State the preparation type.
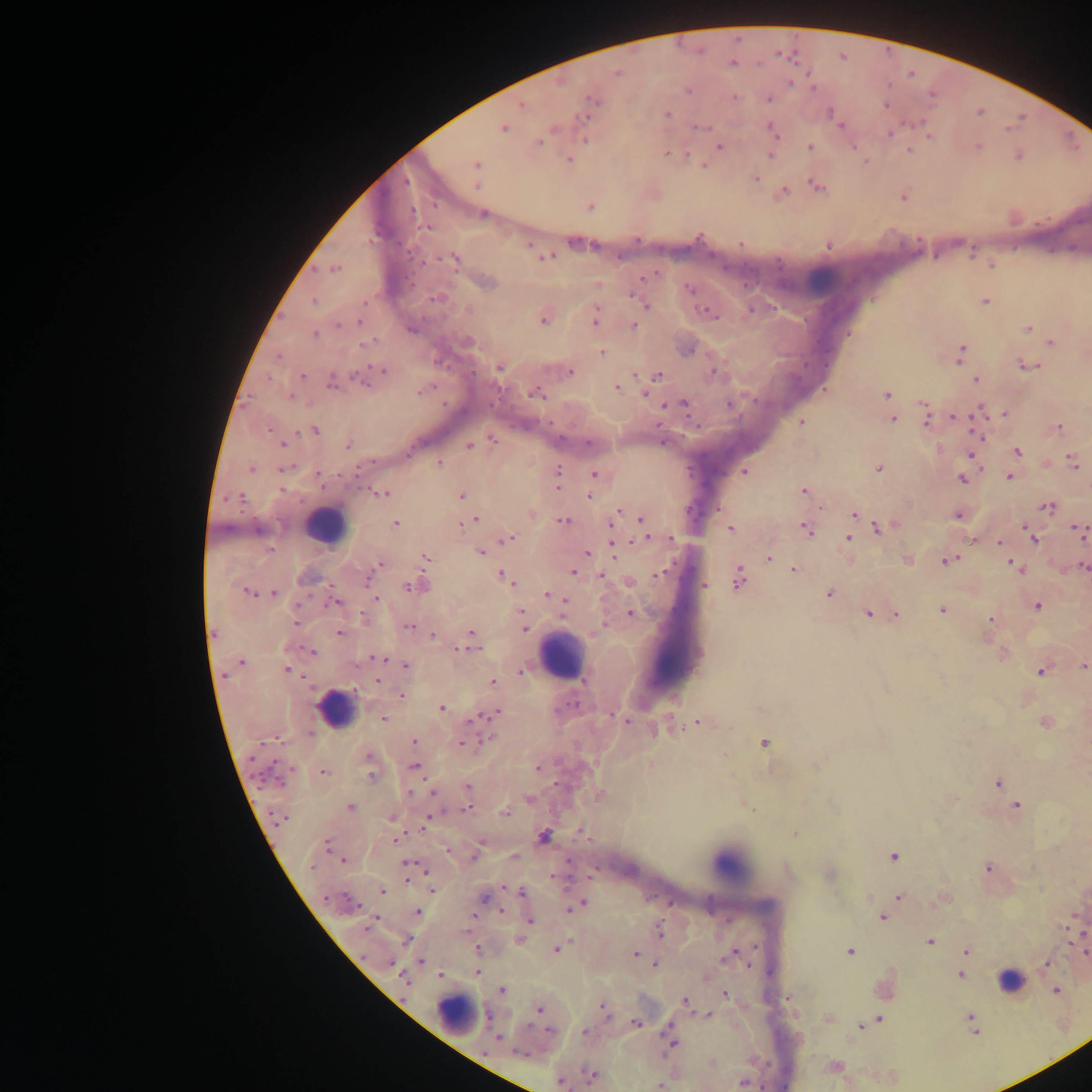

Thick blood film.

Approximate centers as [x, y] in pixels.
Summary:
  - Leukocyte locations: [823, 276], [327, 527], [561, 656], [663, 661], [335, 709], [732, 863], [1008, 979], [457, 1015]
  - Plasmodium parasite locations: [733, 63], [617, 74], [911, 74], [789, 83], [688, 90], [734, 97], [769, 99], [592, 101], [886, 104], [522, 105], [589, 109], [979, 112], [831, 113], [668, 115], [840, 125], [700, 127], [553, 128], [504, 129], [773, 131], [891, 132], [930, 137], [584, 139], [539, 141], [719, 146], [978, 146], [809, 147], [909, 150], [667, 153], [770, 155], [1019, 156], [569, 159], [476, 164], [702, 165], [756, 178], [477, 184], [817, 186], [784, 191], [903, 197], [590, 205], [412, 211], [483, 214], [427, 228], [579, 243], [529, 244], [828, 246], [544, 257], [454, 258], [335, 269], [648, 275], [487, 283], [690, 289], [436, 298], [314, 301], [985, 301], [645, 305], [707, 312], [595, 318], [543, 320], [359, 321], [339, 326], [633, 326], [1028, 328], [412, 329], [314, 334], [468, 341], [366, 343], [1051, 343], [961, 352], [601, 353], [1027, 366], [499, 368], [383, 371], [570, 372], [714, 372], [658, 375], [302, 376], [976, 380], [332, 382], [362, 382], [617, 387], [423, 391], [537, 393], [644, 394], [887, 394], [291, 397], [683, 404], [729, 404], [668, 405], [923, 406], [979, 411], [1005, 414], [892, 418], [955, 418], [926, 421], [800, 422], [1059, 428], [315, 430], [978, 435], [492, 440], [589, 443], [282, 444], [348, 445], [469, 445], [1017, 451], [972, 456], [1072, 462], [440, 464], [251, 469], [282, 469], [878, 469], [744, 472], [558, 474], [595, 474], [1009, 477], [962, 480], [804, 491], [382, 493], [461, 495], [239, 497], [589, 497], [1048, 507], [618, 513], [855, 513], [959, 515], [474, 520], [563, 521], [643, 521], [395, 524], [464, 524], [611, 526], [878, 528], [730, 529], [806, 530], [258, 531], [1080, 533], [849, 538], [508, 539], [647, 539], [671, 539], [1033, 539], [1000, 543], [613, 547], [270, 550], [480, 553], [587, 553], [426, 558], [769, 558], [948, 560], [380, 564], [1083, 566], [1015, 567], [793, 570], [573, 571], [662, 572], [503, 576], [603, 576], [368, 579], [737, 579], [704, 585], [413, 586], [247, 592], [273, 593], [829, 594], [549, 595], [559, 598], [377, 599], [334, 603], [1038, 606], [942, 610], [631, 613], [868, 613], [896, 614], [363, 616], [990, 621], [295, 622], [603, 624], [408, 626], [524, 627], [471, 633], [339, 634], [433, 636], [464, 649], [312, 652], [1002, 654], [378, 658], [242, 662], [405, 666], [1083, 666], [288, 670], [522, 672], [1041, 672], [225, 675], [378, 681], [492, 682], [402, 695], [442, 708], [493, 714], [384, 718], [477, 718], [626, 721], [1045, 722], [698, 723], [489, 739], [415, 741], [764, 743], [463, 744], [369, 756], [414, 766], [538, 768], [324, 772], [372, 777], [277, 780], [998, 783], [468, 787], [412, 792], [434, 793], [529, 799], [1017, 806], [350, 807], [467, 809], [505, 813], [429, 817], [280, 818], [391, 818], [581, 832], [794, 834], [544, 837], [396, 839], [327, 843], [447, 851], [475, 855], [513, 857], [893, 857], [343, 860], [408, 865], [312, 867], [987, 868], [425, 870], [431, 890], [382, 891], [521, 892], [899, 896], [485, 899], [349, 901], [581, 904], [502, 910], [418, 912], [883, 918], [531, 921], [372, 922], [369, 926], [660, 932], [406, 941], [930, 941], [557, 949], [477, 950], [966, 951], [849, 952], [1085, 953], [635, 954], [730, 955], [422, 962], [390, 963], [1046, 963], [655, 965], [477, 972], [440, 975], [961, 975], [404, 980], [502, 989], [1056, 990], [726, 994], [685, 1001], [539, 1009], [604, 1009], [709, 1015], [969, 1017], [878, 1020], [635, 1023], [862, 1026], [549, 1031], [584, 1032], [498, 1037], [671, 1042], [520, 1053], [590, 1075], [561, 1082], [743, 1082], [661, 1086]
  - Country: Ghana
  - Field of view: single
  - Image size: 1092×1092 pixels
  - Capture: mobile-phone photograph through a microscope